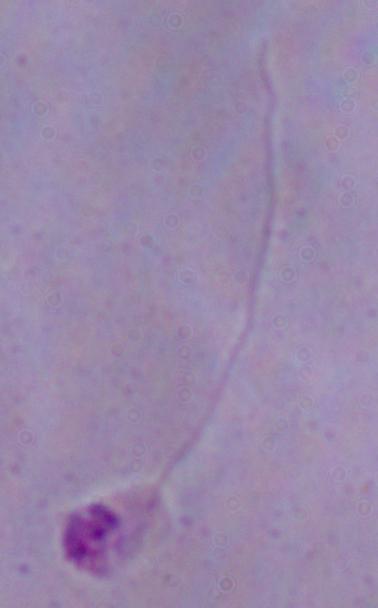

{
  "modality": "micrograph",
  "magnification": "1000x",
  "identification": "Leishmania"
}